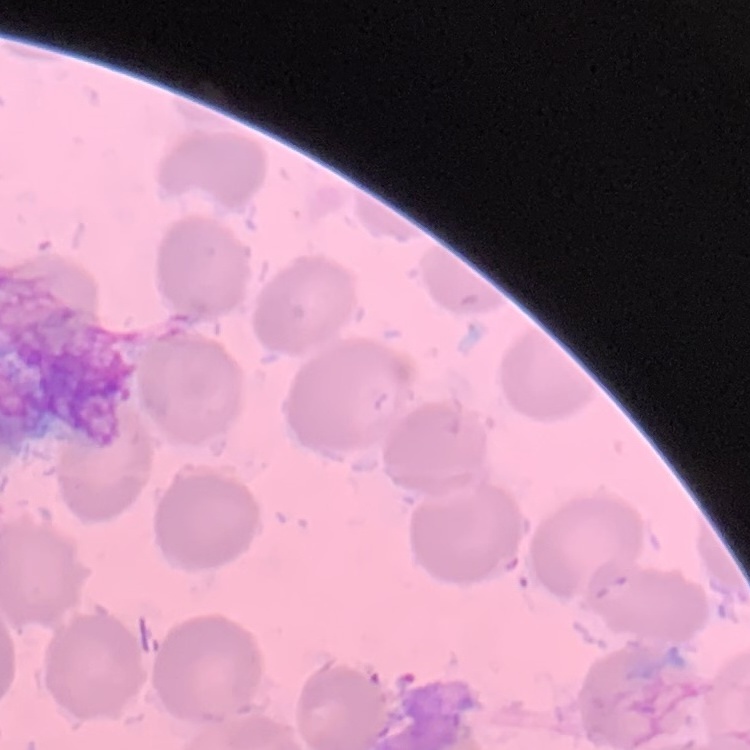 The erythrocytes exhibit no rouleaux formation. Square crop of a larger photomicrograph. Thin peripheral smear. Stained with either Field's or Giemsa.